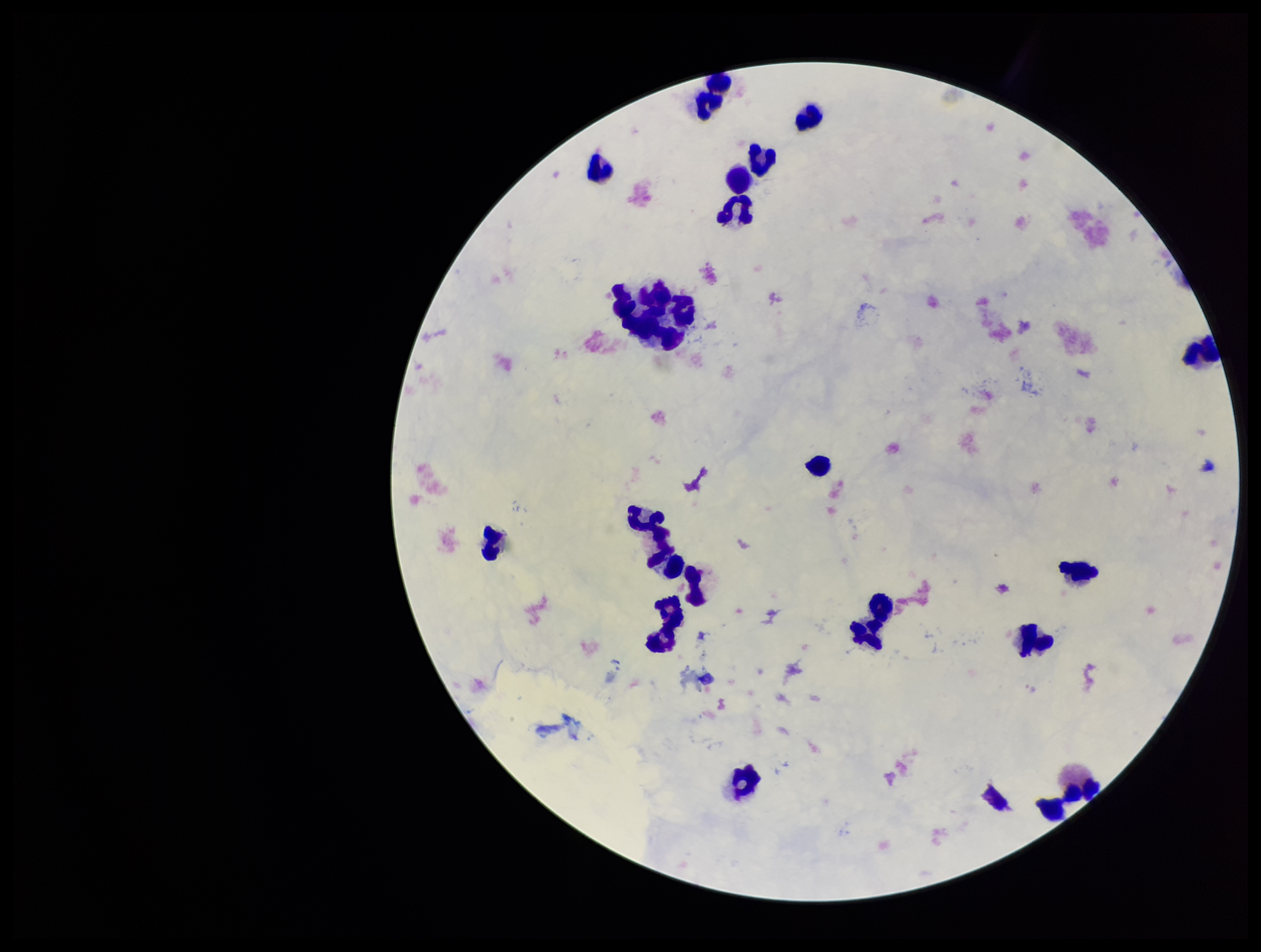
Parasite count: 0. Leukocyte count: 21. Stained with Giemsa. Plasmodium parasites: none identified. Smartphone photograph taken through the eyepiece of a microscope. Single field of view. Patient malaria status: negative. Image is 1261×952 pixels. Preparation: thick smear.